Identify the cell.
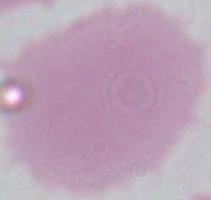

This is an erythrocyte.

Summary:
  - Modality: photomicrograph
  - Magnification: 1000x